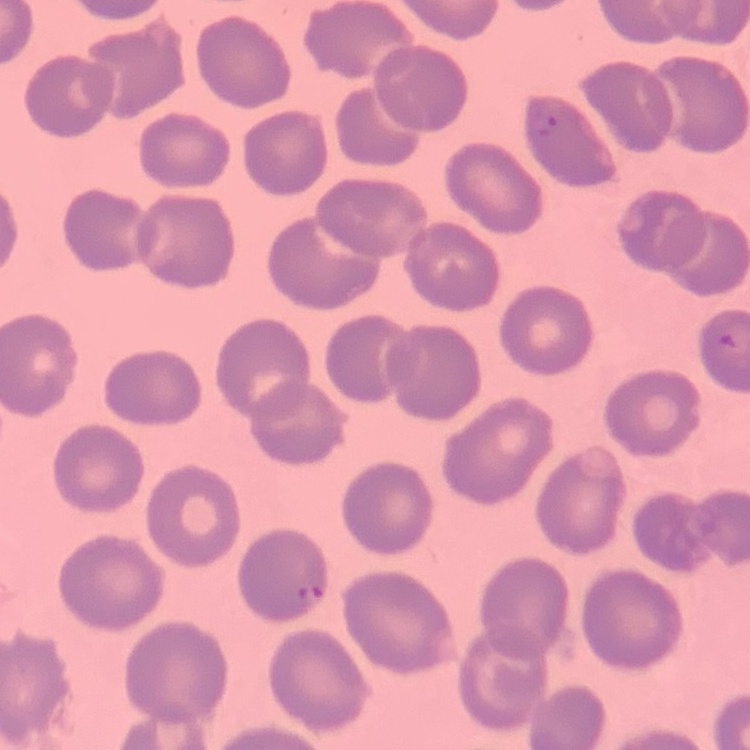

Summary:
  - Red blood cell morphology: no rouleaux formation
  - Preparation: thin blood film
  - Image type: square crop of a larger photomicrograph
  - Stain: Field's or Giemsa